Classify this cell by malaria status.
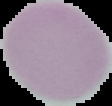

It is uninfected.

preparation = thin blood smear
image size = 112×106 pixels
image type = cell region segmented out of the field of view; surrounding area masked to black